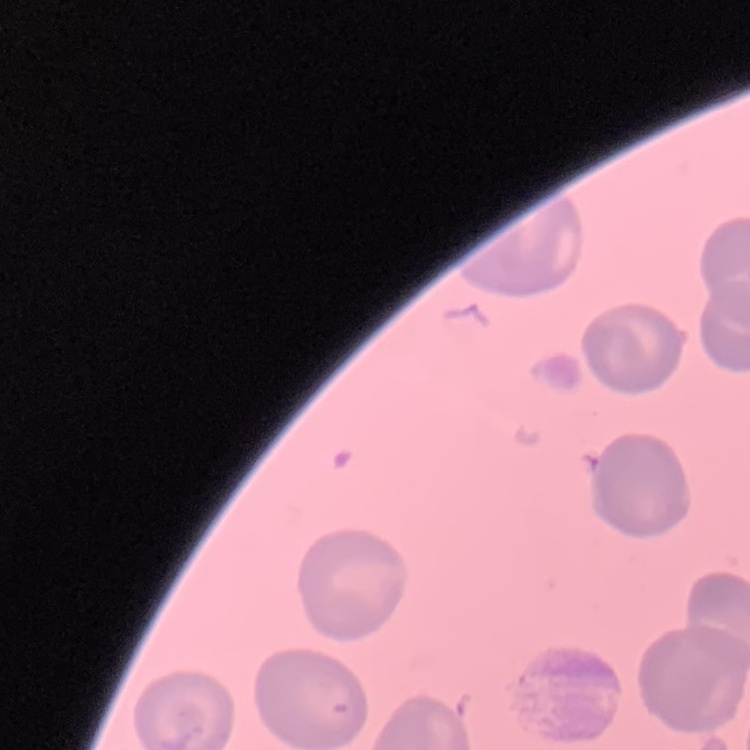

{
  "erythrocyte_morphology": "no rouleaux formation",
  "image_type": "one tile cut from a larger photomicrograph",
  "preparation": "thin blood film",
  "stain": "Field's or Giemsa"
}